Report the malaria status of this cell.
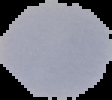
It is parasitized.

From a thin blood smear. Segmented cell region on a black background. Image is 112×100 pixels.